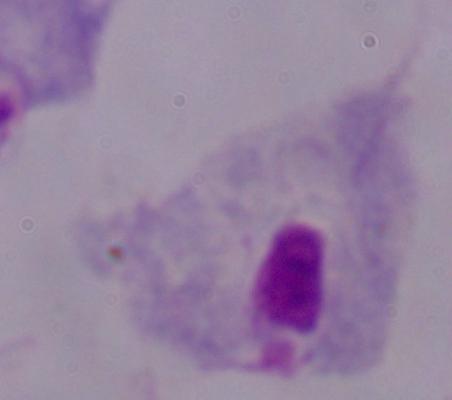
modality = photomicrograph
identification = trichomonad
magnification = 1000x